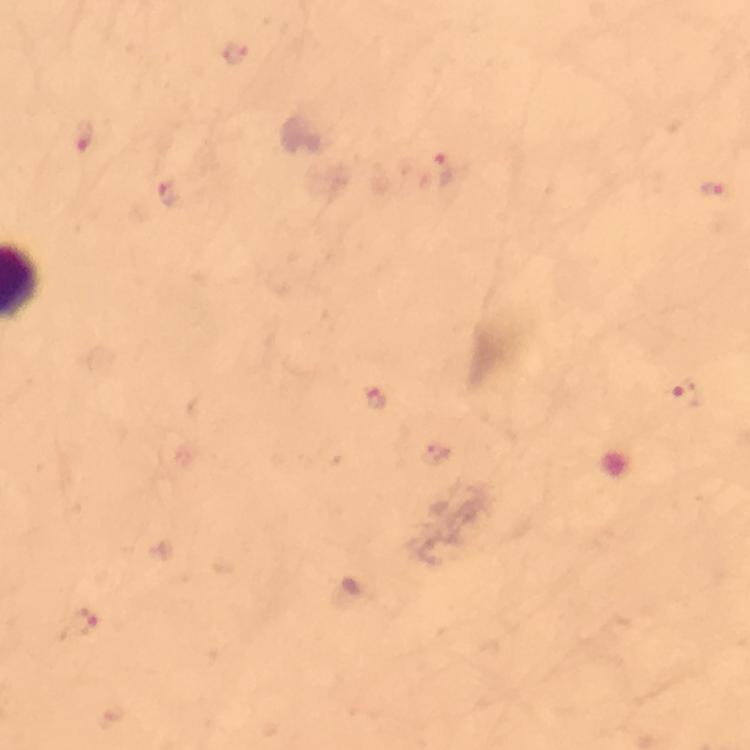

{
  "cropped_from": "a single field of view",
  "immersion_oil": "applied",
  "preparation": "thick smear",
  "image_size": "750×750 pixels",
  "magnification": "100x",
  "plasmodium_parasite_locations": "approximate centers as {x, y} in pixels: {239, 57}, {85, 136}, {438, 175}, {715, 191}, {170, 195}, {686, 397}, {374, 398}, {79, 625}",
  "capture": "smartphone camera through the microscope",
  "stain": "Giemsa",
  "context": "from a malaria diagnostic workup"
}